Report the malaria status of this cell.
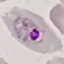

It is parasitized.

preparation = thin smear
stain = Giemsa
capture = smartphone through the microscope eyepiece
image type = cell patch, automatically extracted from a larger field of view and resized to 64 × 64 pixels